Describe the morphology of the red blood cells.
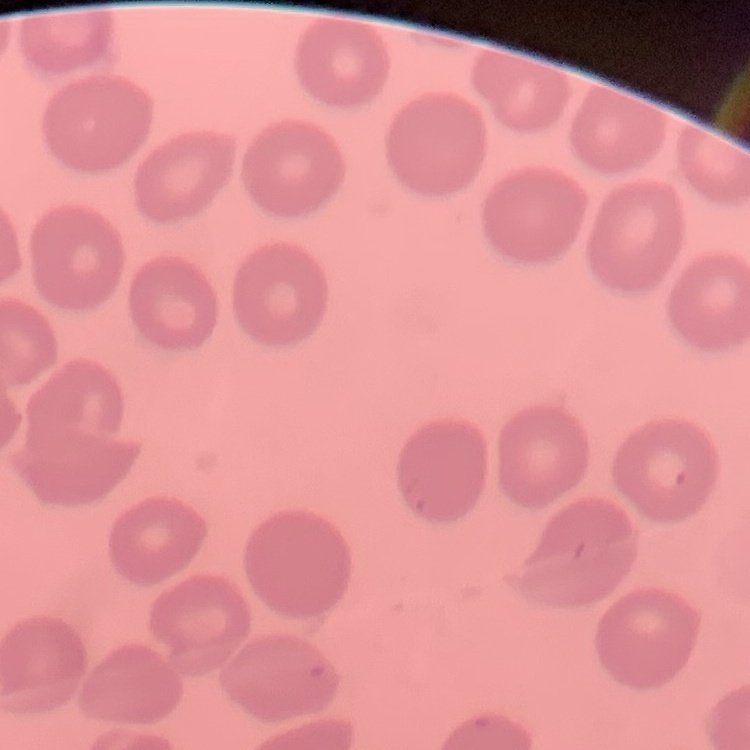

No rouleaux formation.

{
  "preparation": "thin blood film",
  "image_type": "square crop of a larger photomicrograph",
  "stain": "Field's or Giemsa"
}